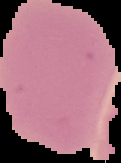
result = no Plasmodium parasites seen
preparation = thin blood film
image size = 121×163 pixels
image type = segmented cell region with the area outside set to black